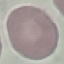
{
  "malaria_status": "uninfected",
  "stain": "Giemsa",
  "preparation": "thin blood film",
  "capture": "smartphone camera at the microscope eyepiece",
  "image_type": "automatically extracted cell patch, resized to 64 × 64 pixels"
}